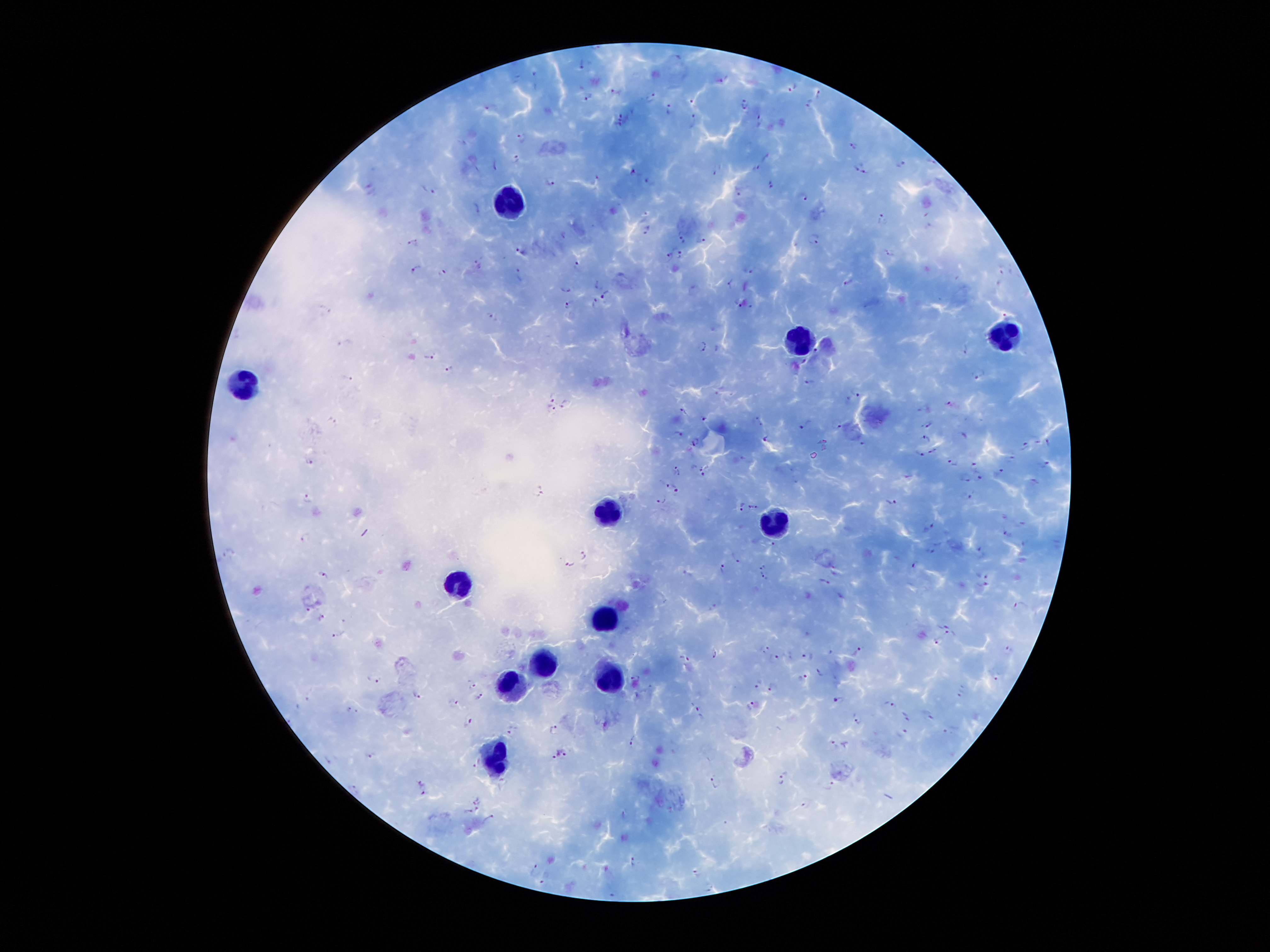
Approximate object centers, in pixels from the top-left corner. Leukocyte locations: (x=511, y=204), (x=1001, y=337), (x=802, y=339), (x=238, y=384), (x=603, y=514), (x=776, y=522), (x=456, y=582), (x=600, y=618), (x=545, y=663), (x=610, y=680), (x=512, y=683), (x=496, y=764). Malaria parasite locations: (x=581, y=64), (x=719, y=80), (x=792, y=86), (x=616, y=90), (x=818, y=94), (x=649, y=96), (x=589, y=97), (x=693, y=100), (x=744, y=102), (x=808, y=103), (x=489, y=108), (x=669, y=108), (x=621, y=114), (x=693, y=119), (x=760, y=119), (x=619, y=126), (x=522, y=136), (x=854, y=146), (x=517, y=158), (x=495, y=164), (x=858, y=164), (x=901, y=164), (x=717, y=168), (x=757, y=168), (x=632, y=169), (x=868, y=170), (x=598, y=178), (x=553, y=181), (x=649, y=181), (x=770, y=183), (x=429, y=188), (x=738, y=189), (x=804, y=195), (x=881, y=219), (x=647, y=228), (x=682, y=233), (x=703, y=236), (x=813, y=239), (x=415, y=243), (x=519, y=251), (x=890, y=252), (x=678, y=254), (x=668, y=256), (x=577, y=265), (x=415, y=266), (x=750, y=269), (x=442, y=274), (x=519, y=275), (x=1002, y=277), (x=847, y=280), (x=596, y=284), (x=727, y=284), (x=568, y=289), (x=606, y=294), (x=594, y=302), (x=737, y=302), (x=568, y=305), (x=489, y=314), (x=1007, y=315), (x=344, y=342), (x=700, y=344), (x=964, y=349), (x=817, y=352), (x=433, y=355), (x=803, y=362), (x=450, y=369), (x=977, y=373), (x=348, y=378), (x=810, y=382), (x=554, y=392), (x=854, y=395), (x=567, y=403), (x=924, y=405), (x=551, y=407), (x=684, y=410), (x=704, y=419), (x=758, y=420), (x=929, y=421), (x=335, y=423), (x=806, y=424), (x=837, y=425), (x=678, y=433), (x=927, y=437), (x=767, y=438), (x=695, y=441), (x=1048, y=442), (x=863, y=443), (x=1026, y=447), (x=933, y=450), (x=920, y=452), (x=309, y=460), (x=973, y=460), (x=953, y=461), (x=1047, y=464), (x=677, y=469), (x=996, y=473), (x=703, y=475), (x=964, y=476), (x=980, y=478), (x=664, y=480), (x=677, y=489), (x=538, y=491), (x=968, y=498), (x=309, y=499), (x=662, y=500), (x=891, y=502), (x=741, y=506), (x=754, y=507), (x=928, y=527), (x=1006, y=531), (x=306, y=539), (x=773, y=544), (x=933, y=551), (x=980, y=551), (x=229, y=554), (x=585, y=556), (x=735, y=557), (x=833, y=563), (x=915, y=563), (x=569, y=565), (x=763, y=566), (x=722, y=567), (x=981, y=573), (x=763, y=575), (x=323, y=576), (x=827, y=582), (x=985, y=586), (x=840, y=596), (x=712, y=604), (x=1019, y=607), (x=311, y=609), (x=321, y=618), (x=944, y=625), (x=950, y=633), (x=339, y=637), (x=937, y=641), (x=766, y=646), (x=858, y=650), (x=1009, y=650), (x=715, y=654), (x=773, y=657), (x=806, y=657), (x=685, y=658), (x=819, y=672), (x=996, y=676), (x=376, y=678), (x=635, y=678), (x=803, y=678), (x=759, y=684), (x=474, y=686), (x=772, y=686), (x=959, y=694), (x=416, y=697), (x=480, y=697), (x=839, y=699), (x=454, y=703), (x=890, y=703), (x=751, y=706), (x=353, y=710), (x=701, y=713), (x=927, y=714), (x=906, y=717), (x=469, y=719), (x=858, y=719), (x=511, y=729), (x=553, y=730), (x=949, y=730), (x=901, y=731), (x=633, y=740), (x=835, y=744), (x=553, y=753), (x=565, y=754), (x=369, y=755), (x=330, y=759), (x=476, y=761), (x=783, y=774), (x=419, y=781), (x=714, y=781), (x=829, y=785), (x=355, y=788), (x=423, y=793), (x=475, y=799), (x=807, y=808), (x=477, y=809), (x=467, y=811), (x=489, y=818), (x=632, y=861), (x=535, y=869), (x=696, y=873), (x=545, y=880), (x=708, y=887), (x=612, y=892). 100x magnification. Thick blood smear. Patient malaria status: infected with Plasmodium falciparum. Image is 1270×952 pixels. Giemsa-stained preparation. Single field of view. Smartphone photograph taken through the microscope eyepiece.